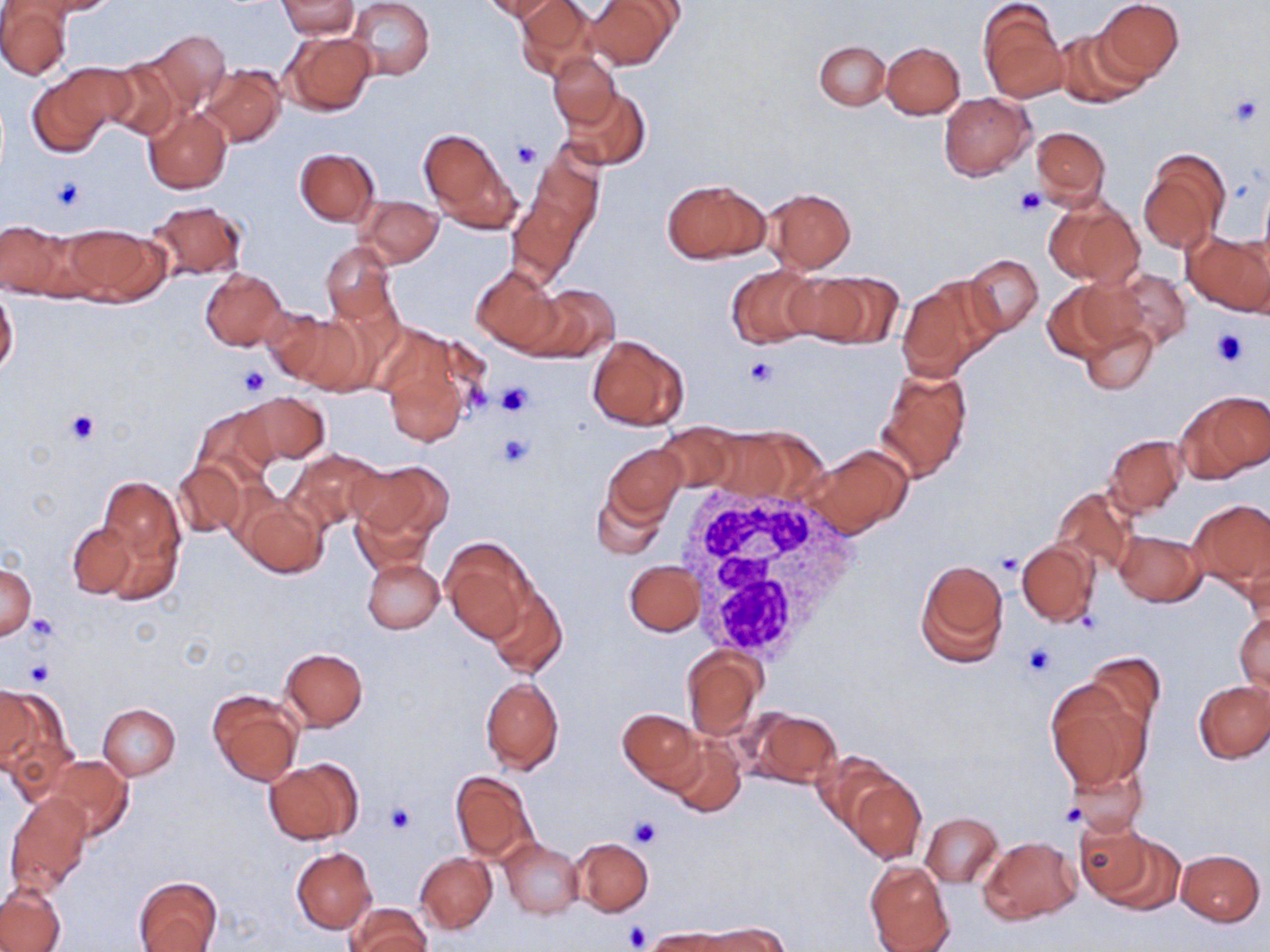
Summary:
  - Coordinate format: approximate bounding boxes as (x1,y1)-(x2,y2) corner pairs in pixels
  - Platelet locations: (1229,94)-(1265,129), (510,141)-(541,170), (50,176)-(86,211), (1014,188)-(1047,217), (1210,326)-(1246,367), (744,356)-(780,388), (238,367)-(272,397), (495,382)-(535,417), (64,410)-(98,443), (496,434)-(534,468), (994,554)-(1021,577), (27,614)-(59,643), (1021,643)-(1058,679), (25,661)-(54,686), (1060,804)-(1084,827), (384,805)-(414,836), (629,817)-(663,850), (623,923)-(651,950)
  - White blood cell locations: (679,479)-(865,664)
  - Uninfected red blood cell locations: (34,0)-(117,16), (275,0)-(360,39), (346,0)-(434,81), (484,0)-(556,22), (515,0)-(596,80), (583,0)-(679,71), (1094,0)-(1184,81), (0,2)-(70,80), (979,3)-(1066,102), (143,29)-(231,109), (1053,29)-(1147,110), (281,31)-(375,116), (815,41)-(890,110), (882,42)-(965,119), (549,53)-(620,131), (100,57)-(186,141), (63,61)-(155,136), (200,65)-(285,148), (28,75)-(114,157), (564,87)-(651,170), (939,93)-(1035,180), (143,107)-(231,194), (1030,126)-(1110,207), (418,128)-(519,231), (510,144)-(602,285), (296,148)-(379,226), (1138,149)-(1229,253), (661,178)-(770,264), (1258,183)-(1270,279), (764,187)-(855,273), (357,195)-(443,268), (1045,197)-(1143,287), (147,200)-(247,280), (0,220)-(74,298), (64,224)-(166,304), (1184,231)-(1270,316), (320,241)-(400,329), (963,254)-(1043,337), (725,264)-(822,348), (471,265)-(562,353), (199,268)-(288,350), (1098,269)-(1191,353), (790,270)-(900,350), (896,275)-(1002,380), (1042,279)-(1134,364), (517,284)-(618,361), (0,289)-(19,376), (260,308)-(364,393), (1078,319)-(1158,396), (587,334)-(690,431), (386,365)-(466,447), (876,367)-(973,483), (1176,389)-(1266,482), (240,392)-(330,466), (190,404)-(279,489), (656,424)-(736,494), (703,429)-(789,502), (1105,434)-(1187,517), (604,444)-(686,522), (806,444)-(913,537), (285,447)-(386,533), (173,462)-(245,538), (349,462)-(453,546), (98,475)-(184,578), (590,485)-(669,560), (1050,485)-(1136,575), (239,497)-(328,580), (1187,497)-(1269,594), (351,499)-(435,577), (66,522)-(136,598), (1115,529)-(1206,607), (442,538)-(532,641), (1017,539)-(1099,626), (1244,545)-(1270,631), (361,557)-(444,634), (915,558)-(1009,667), (626,561)-(702,637), (0,564)-(36,639), (484,583)-(567,679), (1234,610)-(1270,696), (279,647)-(368,730), (682,649)-(763,742), (1083,652)-(1166,738), (480,676)-(564,774), (1193,680)-(1270,765), (1046,681)-(1150,789), (1,685)-(34,767), (1,688)-(76,785), (207,689)-(303,785), (98,704)-(180,780), (617,708)-(703,790), (744,709)-(841,789), (668,736)-(746,817), (45,755)-(134,840), (264,758)-(363,844), (1063,758)-(1150,837), (451,771)-(539,864), (841,773)-(925,864), (6,793)-(92,895), (920,812)-(1002,887), (1078,822)-(1175,909), (979,836)-(1079,925), (570,838)-(653,916), (501,839)-(583,918), (291,847)-(376,932), (1176,849)-(1265,925), (415,853)-(496,933), (864,859)-(955,952), (134,876)-(222,952), (0,884)-(66,951), (346,902)-(430,952), (699,923)-(790,951), (641,928)-(740,952)
  - Slide-level diagnosis: no evidence of blood parasites
  - Modality: light microscopy
  - Stain: May-Grünwald-Giemsa
  - Preparation: thin blood smear
  - Magnification: 1000x
  - Image size: 1270×952 pixels
  - Field of view: one of a larger specimen